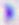
400x magnification. Micrograph. Toxoplasma gondii is shown.